Locate and identify every blood parasite.
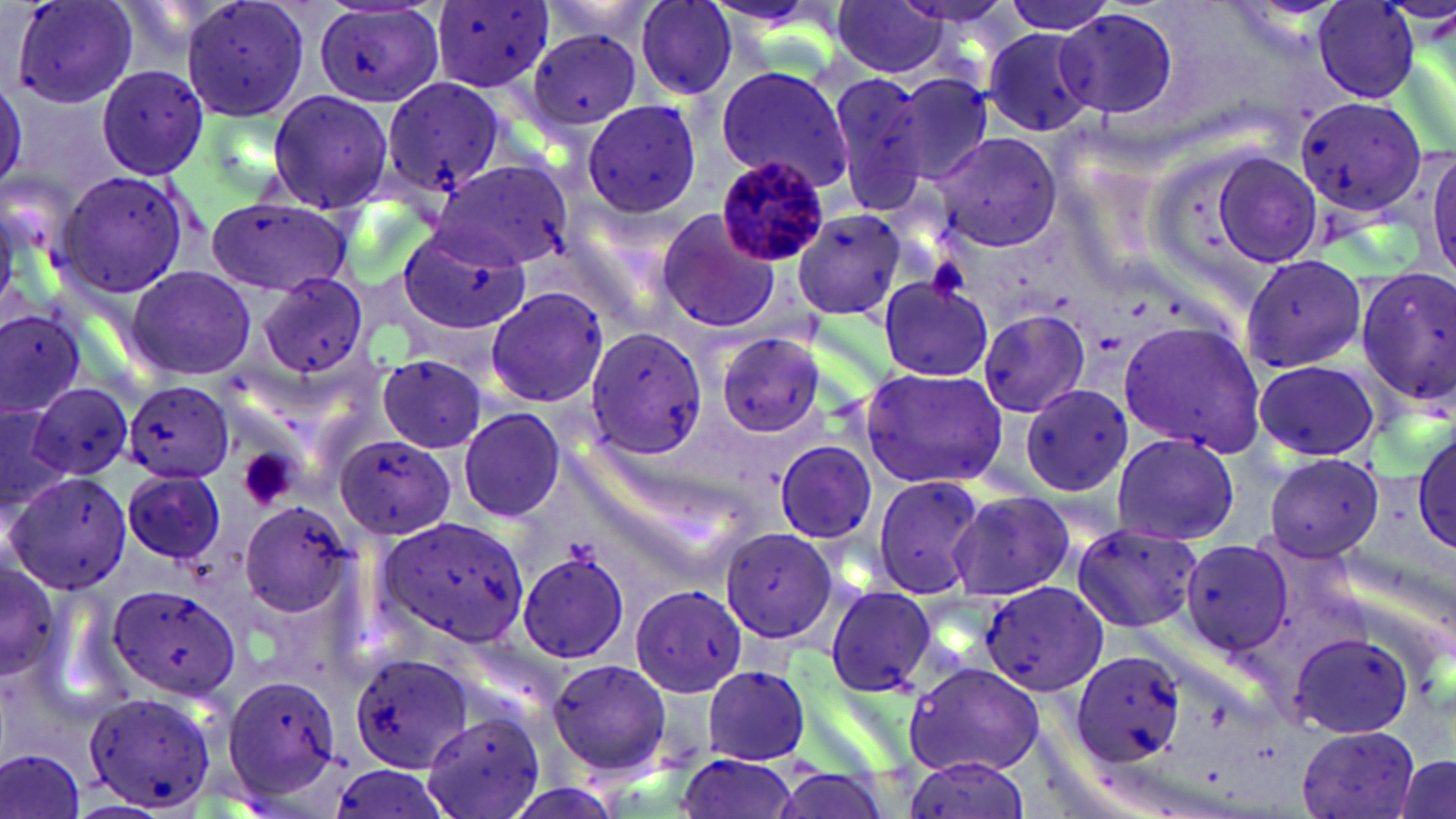

Approximate bounding boxes as [x1, y1, x2, y2] in pixels.
Plasmodium malariae-infected red blood cells: [715, 155, 832, 268].
No Plasmodium falciparum, Plasmodium ovale, Plasmodium vivax, Babesia divergens, or Trypanosoma brucei observed.

{
  "slide_level_diagnosis": "Plasmodium malariae",
  "platelet_locations": "approximate bounding boxes as [x1, y1, x2, y2] in pixels: [927, 256, 973, 299], [238, 449, 296, 511]",
  "magnification": "1000x",
  "stain": "May-Grünwald-Giemsa",
  "image_size": "1456×819 pixels",
  "preparation": "thin blood film",
  "uninfected_red_blood_cell_locations": "approximate bounding boxes as [x1, y1, x2, y2] in pixels: [9, 0, 139, 110], [181, 0, 312, 122], [535, 0, 662, 48], [632, 0, 743, 100], [830, 0, 949, 79], [1000, 0, 1120, 34], [312, 1, 444, 110], [434, 1, 555, 91], [1313, 1, 1423, 102], [1052, 5, 1185, 124], [530, 27, 646, 130], [980, 29, 1096, 136], [96, 63, 213, 178], [714, 66, 851, 192], [381, 74, 508, 200], [827, 74, 932, 215], [892, 74, 993, 186], [265, 90, 396, 211], [1293, 93, 1428, 218], [581, 100, 701, 217], [933, 133, 1063, 252], [1426, 146, 1456, 274], [1211, 153, 1322, 270], [430, 159, 571, 271], [55, 169, 197, 303], [207, 198, 356, 297], [791, 206, 908, 320], [654, 207, 779, 334], [392, 224, 528, 345], [1240, 252, 1368, 374], [1355, 264, 1456, 409], [125, 265, 257, 382], [255, 273, 371, 380], [876, 277, 992, 381], [481, 285, 611, 411], [0, 304, 84, 417], [977, 307, 1092, 420], [1119, 319, 1267, 459], [582, 326, 708, 461], [714, 333, 827, 440], [377, 355, 487, 453], [1250, 358, 1383, 463], [859, 366, 1009, 491], [123, 379, 234, 483], [26, 381, 136, 485], [1018, 384, 1133, 497], [0, 405, 67, 507], [458, 407, 567, 524], [1411, 428, 1456, 557], [1109, 433, 1240, 547], [334, 434, 458, 541], [773, 440, 878, 544], [1261, 452, 1386, 562], [121, 469, 227, 565], [5, 473, 127, 595], [871, 474, 987, 602], [949, 489, 1074, 600], [238, 499, 356, 619], [375, 513, 535, 651], [1069, 522, 1202, 633], [719, 526, 840, 644], [1181, 540, 1295, 655], [517, 548, 633, 662], [0, 554, 67, 688], [979, 581, 1109, 696], [631, 583, 748, 696], [107, 584, 242, 700], [825, 585, 937, 696], [1288, 631, 1413, 740], [1070, 647, 1186, 768], [348, 653, 474, 773], [546, 657, 670, 780], [906, 662, 1045, 778], [702, 666, 811, 764], [220, 674, 342, 803], [81, 687, 223, 811], [421, 709, 548, 819], [1295, 724, 1419, 819], [0, 746, 89, 819], [672, 755, 799, 819], [902, 755, 1029, 819], [1390, 755, 1454, 819], [757, 761, 902, 819]",
  "modality": "optical microscopy",
  "field_of_view": "single"
}